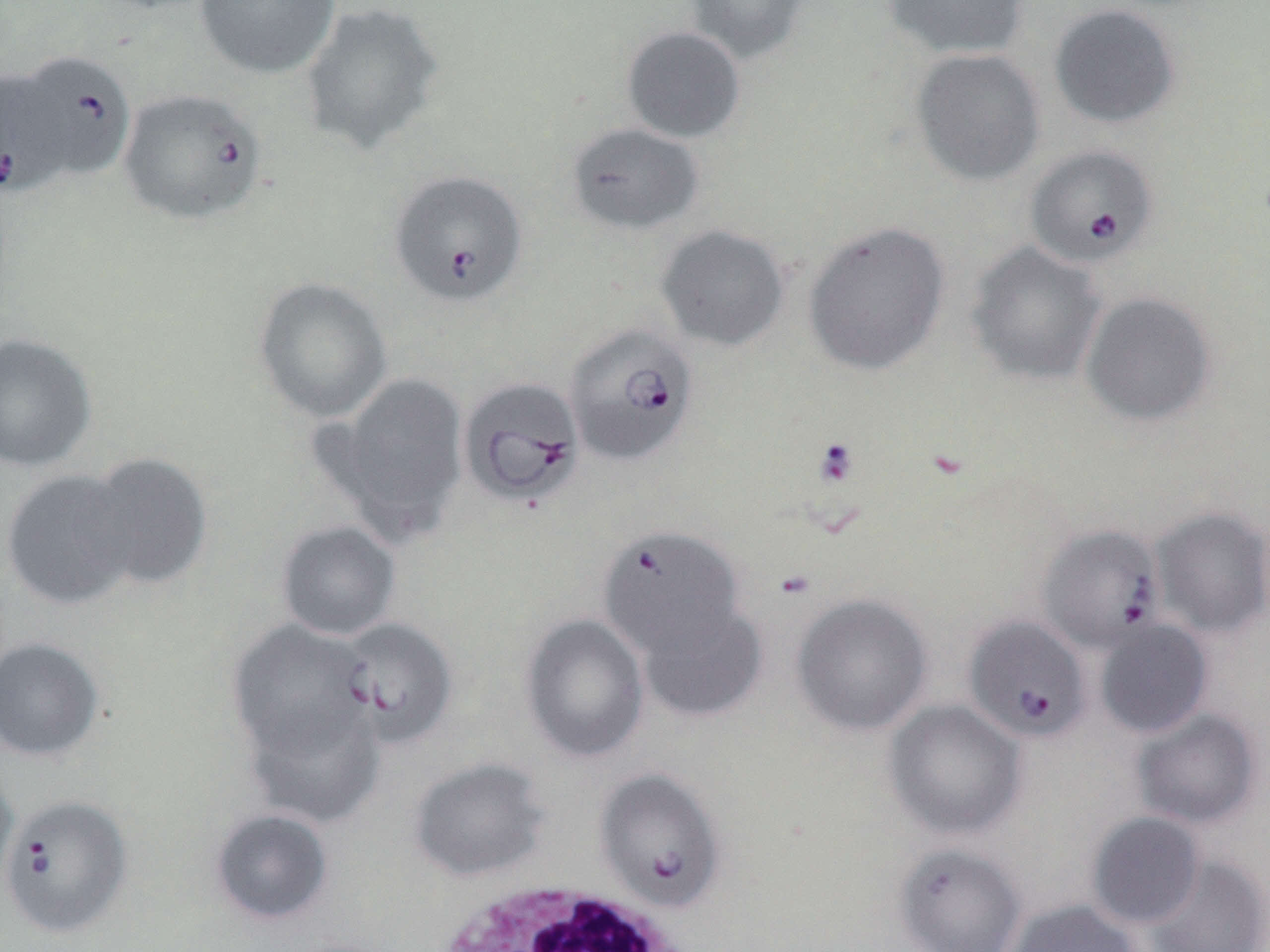
Summary:
  - Coordinate format: approximate bounding boxes as (x1, y1, x2, y2) in pixels
  - Babesia divergens-infected red blood cell locations: (17, 49, 136, 181), (0, 69, 68, 196), (118, 87, 267, 226), (1025, 146, 1158, 266), (388, 171, 528, 308), (564, 323, 698, 465), (457, 377, 585, 510), (1036, 524, 1166, 653), (597, 525, 745, 660), (964, 616, 1092, 744), (336, 618, 458, 749), (594, 768, 727, 914), (0, 794, 133, 938)
  - White blood cell locations: (433, 882, 692, 952)
  - Uninfected red blood cell locations: (195, 0, 340, 79), (684, 0, 811, 65), (882, 0, 1030, 60), (300, 2, 445, 157), (1049, 4, 1182, 129), (621, 25, 745, 143), (910, 49, 1046, 186), (567, 123, 704, 236), (803, 220, 951, 376), (656, 225, 790, 351), (965, 242, 1105, 386), (253, 277, 392, 423), (1080, 291, 1218, 427), (0, 332, 97, 473), (322, 372, 470, 541), (80, 452, 213, 591), (1, 468, 141, 610), (1152, 507, 1270, 637), (276, 520, 402, 640), (791, 593, 933, 736), (636, 601, 768, 723), (519, 612, 650, 763), (1095, 618, 1214, 739), (227, 622, 373, 757), (0, 637, 106, 763), (243, 697, 384, 827), (884, 699, 1027, 840), (1132, 709, 1263, 829), (408, 757, 550, 882), (0, 769, 18, 902), (209, 808, 334, 927), (1086, 812, 1205, 929), (893, 843, 1027, 952), (1143, 853, 1269, 952), (1005, 899, 1144, 952)
  - Slide-level diagnosis: Babesia divergens
  - Preparation: thin blood film
  - Modality: light microscopy
  - Image size: 1270×952 pixels
  - Magnification: 1000x
  - Stain: May-Grünwald-Giemsa
  - Field of view: single